Assess the morphology of the red blood cells.
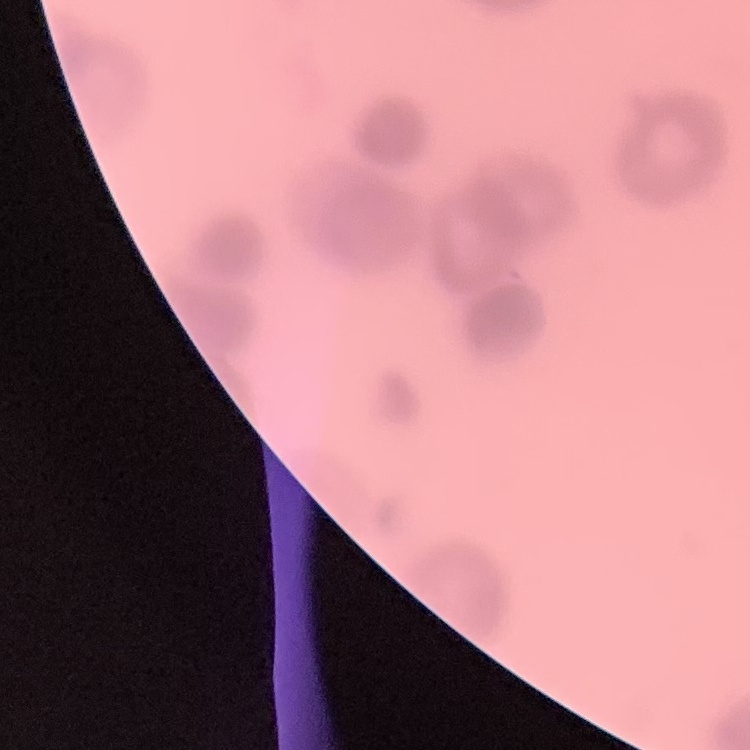
Rouleaux formation.

Field's or Giemsa stain. One tile cut from a larger photomicrograph. Thin blood smear.